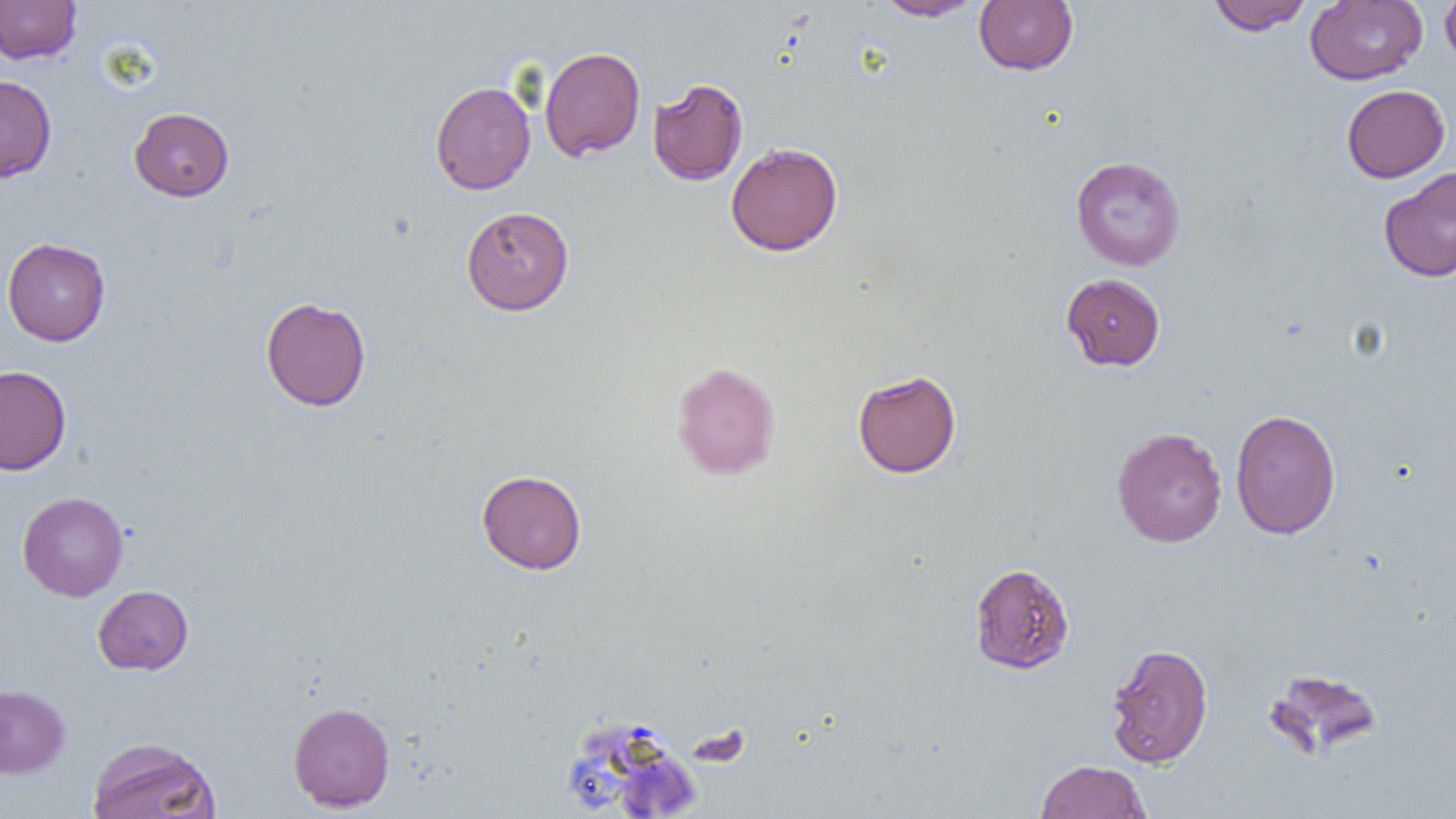

slide_level_diagnosis: no evidence of blood parasites
magnification: 1000x
uninfected_red_blood_cell_locations: 'approximate bounding boxes as (x1,y1)-(x2,y2) corner pairs in pixels: (874,0)-(984,21), (973,0)-(1078,75), (1206,0)-(1312,35), (1305,0)-(1427,85), (1440,0)-(1456,67), (0,1)-(81,65), (540,46)-(646,163), (0,75)-(57,183), (648,77)-(748,186), (430,81)-(536,194), (1341,84)-(1450,182), (129,107)-(234,201), (725,141)-(843,256), (1070,155)-(1185,271), (1378,166)-(1456,282), (461,206)-(574,315), (2,237)-(111,346), (1061,273)-(1166,371), (260,297)-(371,411), (671,361)-(781,480), (0,365)-(71,475), (852,369)-(961,478), (1230,408)-(1340,540), (1111,426)-(1227,548), (476,469)-(587,575), (17,491)-(129,602), (969,562)-(1075,674), (93,585)-(193,675), (1105,643)-(1213,768), (1262,666)-(1385,761), (0,684)-(70,778), (288,701)-(395,812), (87,736)-(221,819), (1035,759)-(1152,819)'
image_size: 1456×819 pixels
modality: light microscopy
field_of_view: single
preparation: thin blood smear